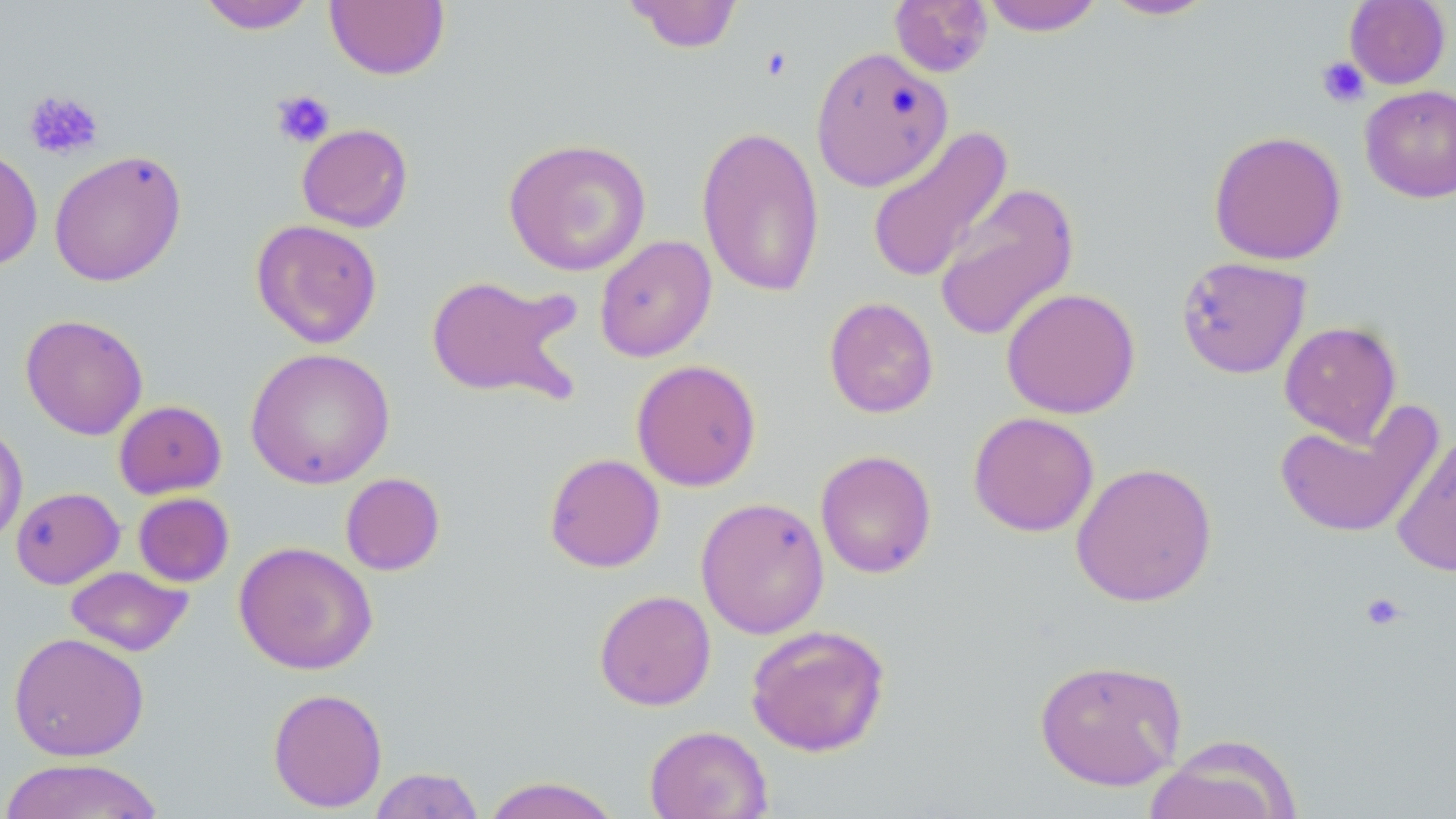 Approximate bounding boxes as [x1, y1, x2, y2] in pixels. Platelet locations: [760, 46, 793, 82], [1316, 56, 1370, 108], [23, 89, 103, 161], [270, 89, 335, 148], [1359, 592, 1408, 631]. Uninfected red blood cell locations: [622, 0, 744, 54], [889, 0, 993, 78], [980, 0, 1104, 35], [1100, 0, 1219, 20], [1344, 0, 1451, 89], [196, 1, 317, 34], [325, 1, 450, 80], [810, 46, 953, 191], [1360, 84, 1456, 203], [297, 123, 413, 233], [695, 124, 826, 298], [865, 126, 1014, 284], [1208, 130, 1347, 265], [503, 137, 652, 276], [0, 147, 43, 271], [49, 149, 187, 287], [933, 183, 1080, 342], [251, 219, 383, 349], [594, 235, 717, 362], [1175, 256, 1312, 379], [424, 274, 583, 404], [1001, 287, 1140, 419], [824, 296, 939, 418], [20, 314, 148, 440], [1279, 320, 1403, 445], [245, 347, 395, 489], [630, 359, 762, 491], [113, 400, 227, 499], [1274, 404, 1442, 540], [967, 411, 1100, 537], [0, 422, 28, 546], [1392, 431, 1456, 579], [814, 449, 937, 579], [544, 453, 666, 572], [1070, 461, 1218, 607], [340, 472, 446, 576], [10, 487, 125, 589], [133, 493, 234, 587], [695, 496, 830, 639], [234, 541, 377, 675], [65, 566, 193, 657], [593, 589, 716, 711], [746, 624, 891, 757], [8, 631, 149, 761], [1033, 658, 1188, 791], [267, 687, 388, 813], [644, 725, 773, 819], [1145, 735, 1302, 819], [1, 757, 166, 819], [367, 767, 486, 818], [480, 776, 623, 819]. Slide-level diagnosis: no evidence of blood parasites. Single field of view. 1000x magnification. Thin blood film. Optical microscopy. May-Grünwald-Giemsa stain. Image is 1456×819 pixels.